State which cell type is depicted.
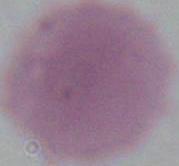

An erythrocyte.

1000x magnification. Photomicrograph.